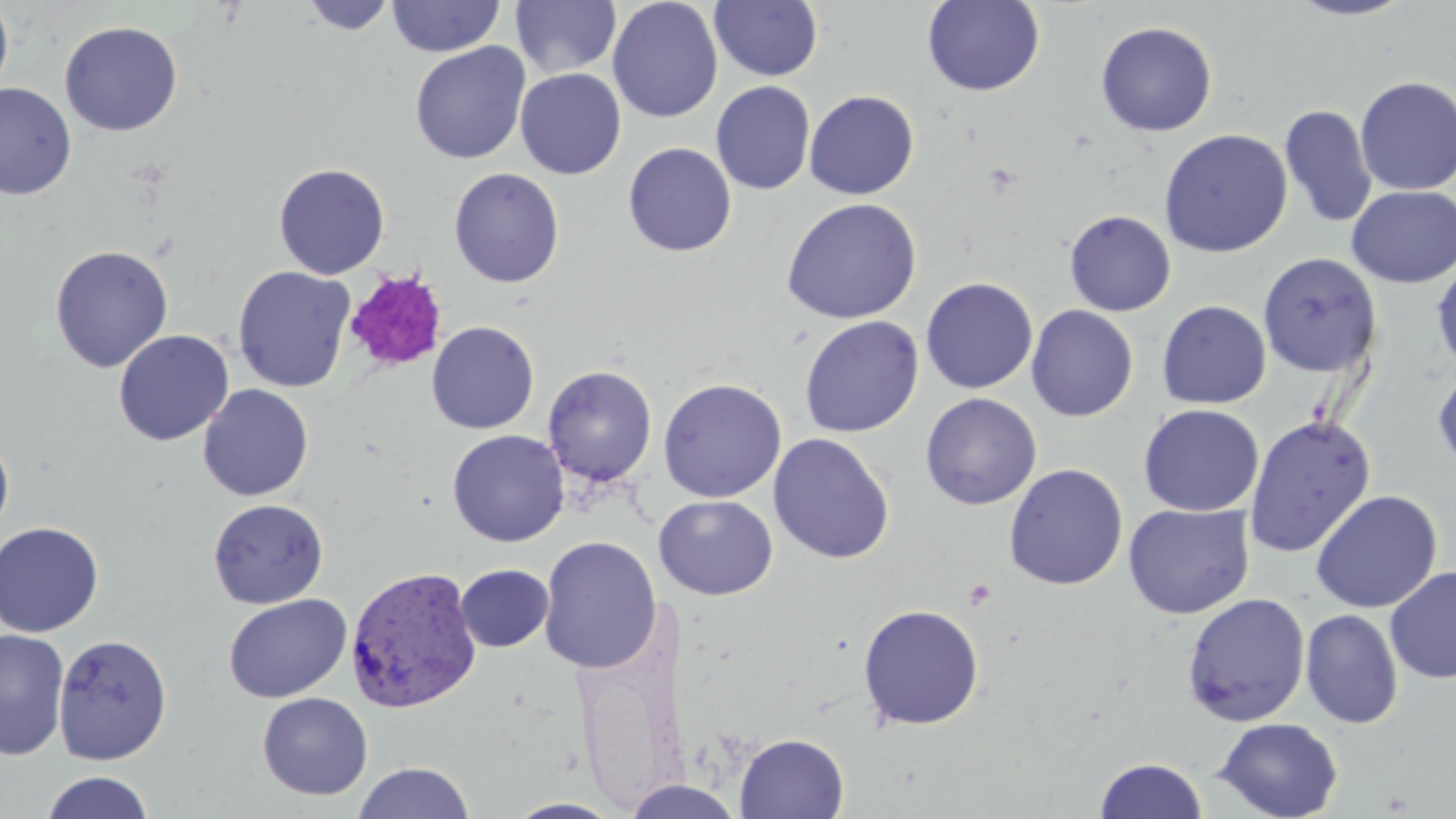

{
  "slide_level_diagnosis": "Plasmodium vivax",
  "uninfected_red_blood_cell_locations": "approximate bounding boxes as named x1/y1/x2/y2 corners in pixels: (x1=0, y1=0, x2=14, y2=102), (x1=299, y1=0, x2=397, y2=35), (x1=386, y1=0, x2=505, y2=58), (x1=922, y1=0, x2=1045, y2=96), (x1=1286, y1=0, x2=1416, y2=22), (x1=511, y1=1, x2=622, y2=80), (x1=607, y1=1, x2=723, y2=122), (x1=709, y1=1, x2=823, y2=82), (x1=59, y1=21, x2=183, y2=137), (x1=1096, y1=21, x2=1218, y2=137), (x1=409, y1=41, x2=531, y2=164), (x1=515, y1=68, x2=627, y2=179), (x1=1354, y1=76, x2=1456, y2=196), (x1=711, y1=80, x2=816, y2=195), (x1=0, y1=82, x2=76, y2=200), (x1=804, y1=90, x2=919, y2=199), (x1=1279, y1=104, x2=1377, y2=229), (x1=1158, y1=128, x2=1293, y2=258), (x1=623, y1=142, x2=737, y2=256), (x1=274, y1=163, x2=390, y2=279), (x1=448, y1=167, x2=565, y2=288), (x1=1346, y1=185, x2=1456, y2=288), (x1=782, y1=197, x2=921, y2=324), (x1=1064, y1=209, x2=1176, y2=316), (x1=49, y1=244, x2=174, y2=372), (x1=1257, y1=252, x2=1382, y2=378), (x1=1432, y1=258, x2=1456, y2=376), (x1=233, y1=266, x2=356, y2=393), (x1=920, y1=277, x2=1038, y2=394), (x1=1157, y1=300, x2=1271, y2=409), (x1=1026, y1=305, x2=1138, y2=422), (x1=799, y1=316, x2=923, y2=437), (x1=426, y1=321, x2=539, y2=434), (x1=114, y1=330, x2=233, y2=446), (x1=542, y1=365, x2=658, y2=488), (x1=1433, y1=366, x2=1456, y2=474), (x1=658, y1=377, x2=787, y2=503), (x1=198, y1=383, x2=313, y2=501), (x1=920, y1=392, x2=1042, y2=510), (x1=1138, y1=403, x2=1264, y2=517), (x1=1243, y1=414, x2=1376, y2=558), (x1=447, y1=429, x2=569, y2=547), (x1=0, y1=430, x2=14, y2=542), (x1=769, y1=433, x2=894, y2=564), (x1=1004, y1=463, x2=1128, y2=590), (x1=1310, y1=490, x2=1442, y2=613), (x1=653, y1=495, x2=778, y2=600), (x1=208, y1=498, x2=329, y2=608), (x1=1123, y1=503, x2=1254, y2=619), (x1=0, y1=521, x2=104, y2=637), (x1=538, y1=535, x2=662, y2=675), (x1=454, y1=564, x2=554, y2=652), (x1=1384, y1=565, x2=1456, y2=684), (x1=1182, y1=592, x2=1310, y2=727), (x1=223, y1=594, x2=352, y2=703), (x1=858, y1=603, x2=985, y2=730), (x1=1300, y1=608, x2=1403, y2=729), (x1=0, y1=629, x2=70, y2=761), (x1=53, y1=633, x2=173, y2=765), (x1=257, y1=692, x2=373, y2=800), (x1=1213, y1=716, x2=1343, y2=819), (x1=735, y1=733, x2=849, y2=818), (x1=1095, y1=757, x2=1208, y2=818), (x1=352, y1=761, x2=475, y2=818), (x1=39, y1=771, x2=155, y2=819), (x1=622, y1=779, x2=745, y2=817), (x1=503, y1=798, x2=626, y2=818)",
  "magnification": "1000x",
  "platelet_locations": "approximate bounding boxes as named x1/y1/x2/y2 corners in pixels: (x1=343, y1=270, x2=448, y2=373), (x1=963, y1=579, x2=996, y2=610)",
  "stain": "May-Grünwald-Giemsa",
  "preparation": "thin blood smear",
  "image_size": "1456×819 pixels",
  "plasmodium_vivax_infected_red_blood_cell_locations": "approximate bounding boxes as named x1/y1/x2/y2 corners in pixels: (x1=344, y1=565, x2=482, y2=715)",
  "modality": "optical microscopy",
  "field_of_view": "single"
}